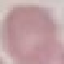

result = no malaria parasites detected
capture = smartphone camera at the microscope eyepiece
preparation = thin blood film
image type = cell patch, automatically extracted from a larger field of view and resized to 64 × 64 pixels
stain = Giemsa